Assess this cell for malaria.
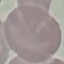
It is uninfected.

preparation: thin blood smear
stain: Giemsa
capture: smartphone through the microscope eyepiece
image_type: cell patch, automatically extracted from a larger field of view and resized to 64 × 64 pixels